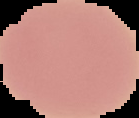
image size = 139×118 pixels
preparation = thin blood smear
malaria status = uninfected
image type = segmented cell region with the area outside set to black